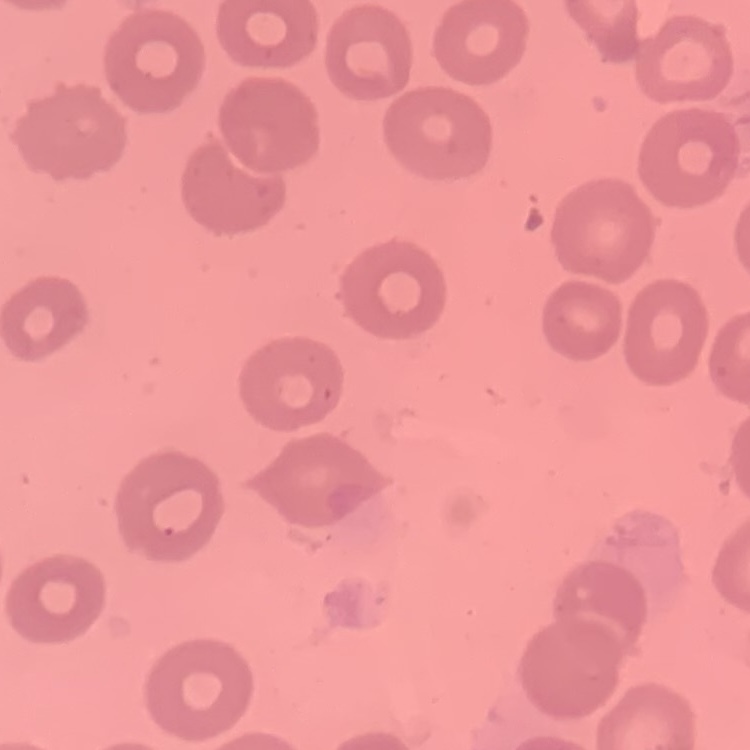

red_blood_cell_morphology: no rouleaux formation
image_type: square crop of a larger photomicrograph
preparation: thin blood smear
stain: Field's or Giemsa